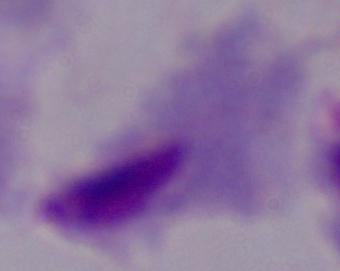

Micrograph. Captured at 1000x magnification. A trichomonad is seen.